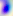
Summary:
  - Magnification: 400x
  - Modality: micrograph
  - Identification: Toxoplasma gondii